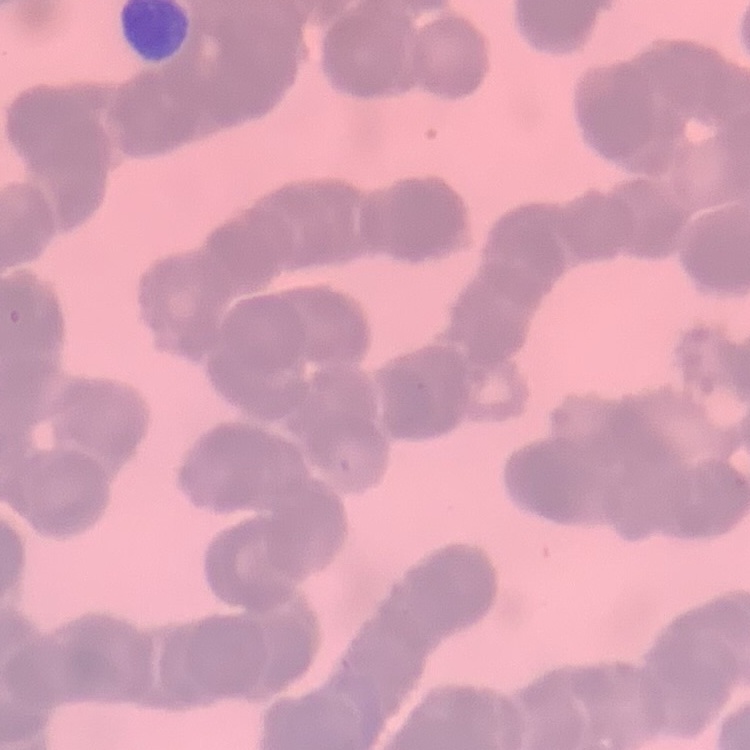

red blood cell morphology = rouleaux formation
preparation = thin blood film
image type = one tile cut from a larger photomicrograph
stain = Field's or Giemsa